Describe the morphology of the red blood cells.
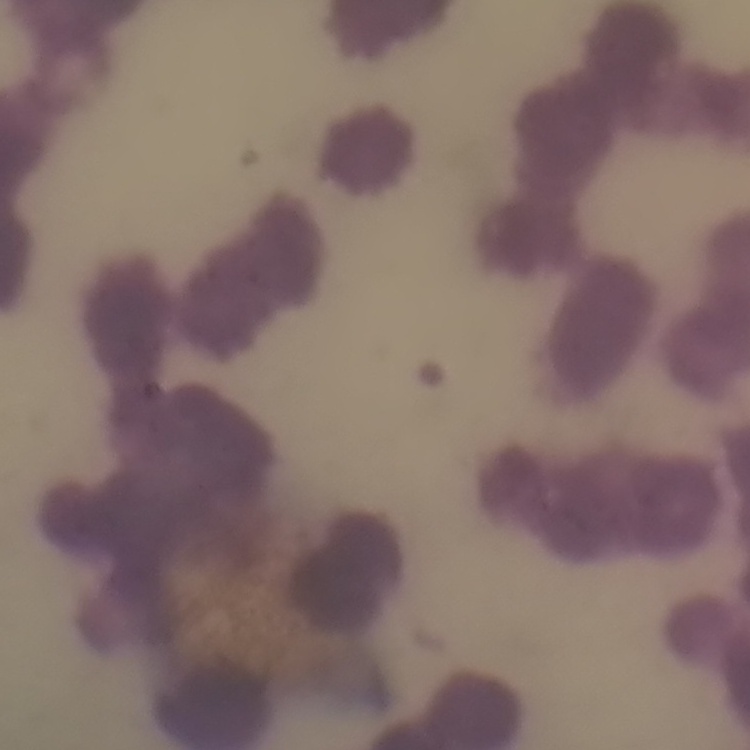
Rouleaux formation.

Summary:
  - Image type: square crop of a larger photomicrograph
  - Stain: Field's or Giemsa
  - Preparation: thin peripheral smear